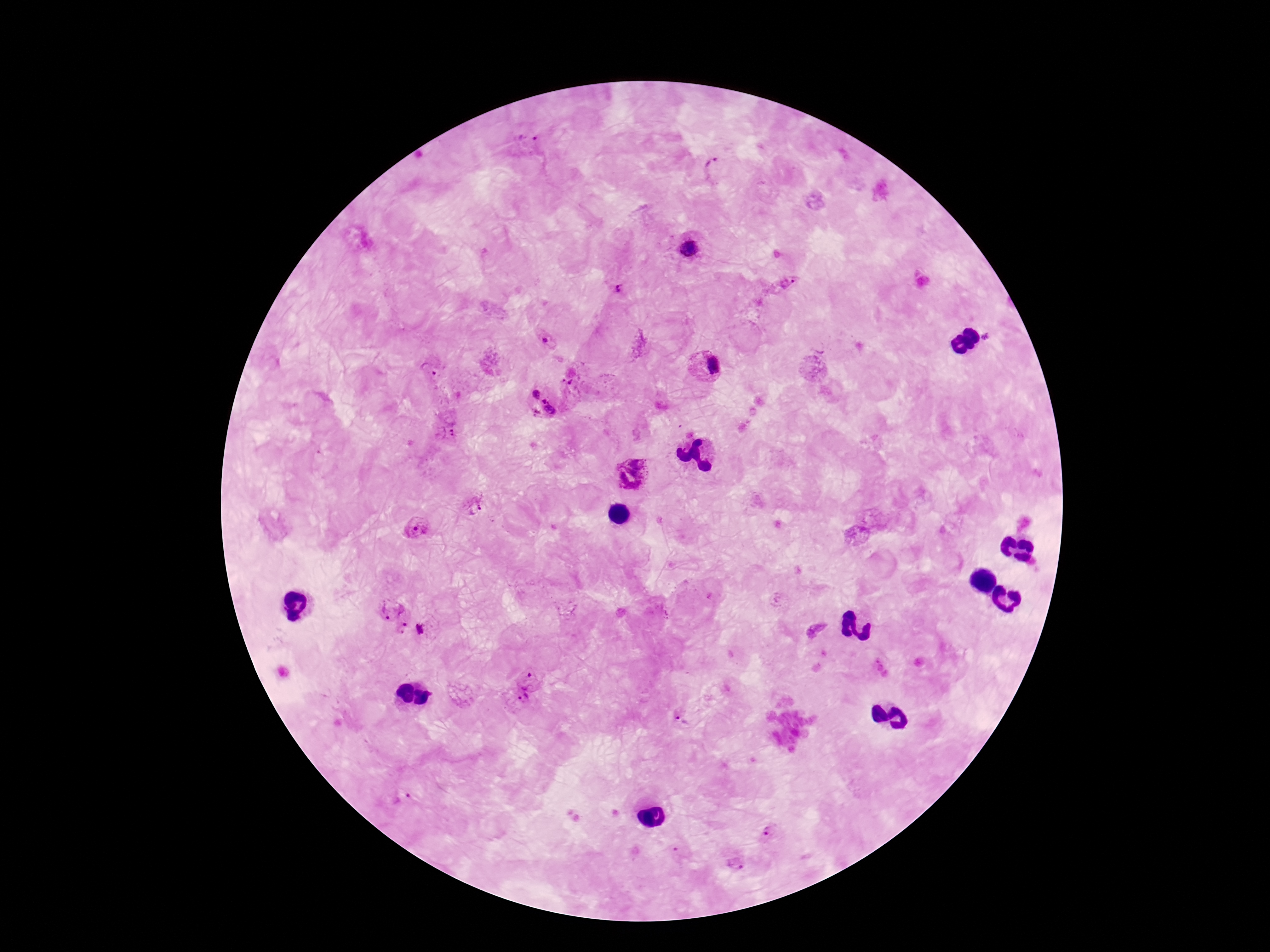

Approximate object centers, in pixels from the top-left corner.
Summary:
  - Plasmodium parasite locations: (x=527, y=143), (x=717, y=167), (x=689, y=244), (x=790, y=283), (x=617, y=288), (x=547, y=340), (x=429, y=368), (x=707, y=369), (x=542, y=403), (x=448, y=433), (x=632, y=474), (x=476, y=503), (x=413, y=525), (x=390, y=605), (x=402, y=627), (x=423, y=629), (x=529, y=674), (x=519, y=702), (x=682, y=718), (x=400, y=796), (x=769, y=833), (x=737, y=863)
  - Capture: smartphone camera through the microscope eyepiece
  - Magnification: 100x
  - Field of view: single
  - Preparation: thick blood film
  - Image size: 1270×952 pixels
  - Stain: Giemsa
  - Patient malaria status: infected